Outline every malaria parasite.
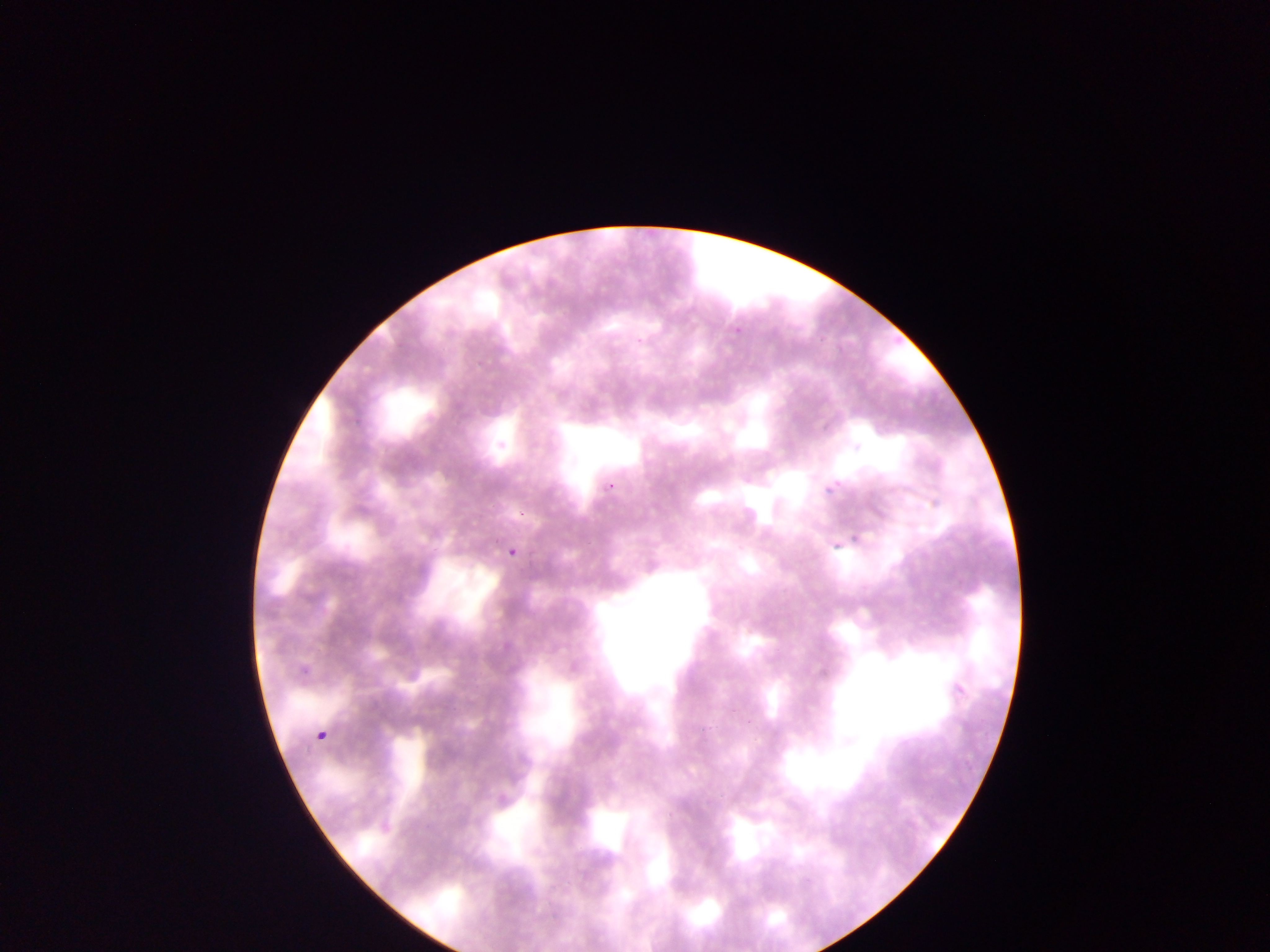
Approximate bounding boxes as {left, top, right, bottom} in pixels.
Malaria parasites: {732, 321, 745, 333}, {634, 332, 650, 347}, {603, 481, 614, 492}, {820, 482, 838, 498}, {516, 509, 533, 520}, {847, 529, 862, 546}, {504, 534, 527, 561}, {833, 541, 842, 549}, {299, 663, 312, 676}, {317, 729, 330, 749}.

Summary:
  - Capture: mobile-phone photograph through a microscope
  - Field of view: single
  - Country: Ghana
  - Preparation: thin blood smear
  - Image size: 1270×952 pixels